Identify the blood parasite species.
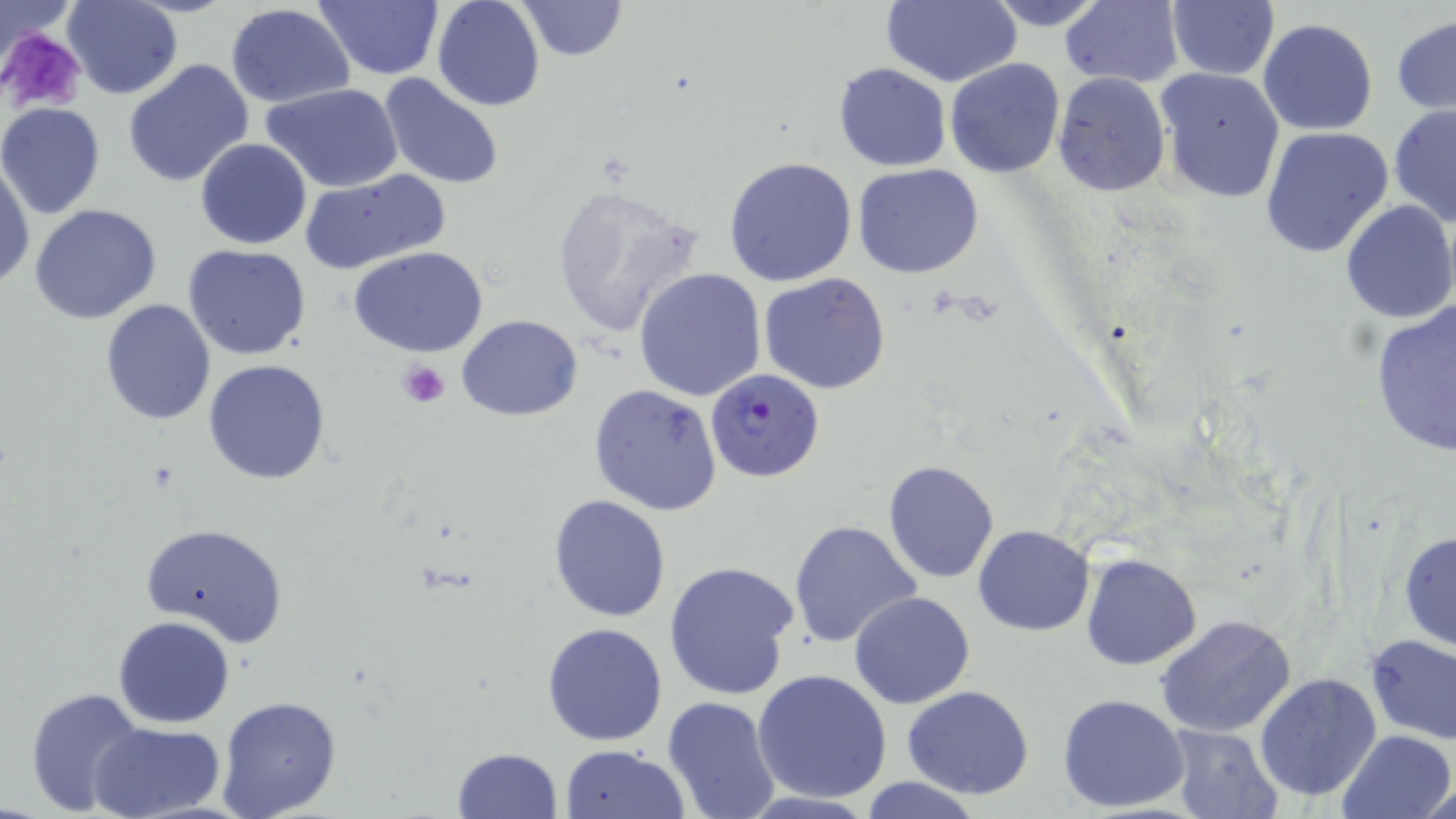

Plasmodium falciparum.

uninfected_red_blood_cell_locations: 'approximate bounding boxes as (x1, y1, x2, y2) in pixels: (315, 0, 443, 79), (432, 0, 545, 111), (517, 0, 627, 61), (883, 0, 1023, 86), (978, 0, 1115, 30), (1060, 0, 1183, 86), (63, 1, 181, 99), (1166, 2, 1280, 79), (225, 4, 355, 108), (1391, 16, 1455, 116), (1257, 18, 1379, 135), (944, 58, 1066, 177), (121, 59, 255, 189), (833, 64, 951, 171), (1153, 67, 1286, 204), (377, 73, 505, 192), (1052, 73, 1171, 198), (263, 83, 406, 194), (0, 103, 106, 219), (1388, 104, 1456, 230), (1260, 126, 1394, 257), (194, 139, 312, 250), (0, 156, 35, 292), (724, 156, 859, 286), (851, 162, 986, 278), (297, 169, 450, 275), (548, 183, 702, 338), (1339, 200, 1455, 323), (28, 203, 162, 324), (183, 245, 311, 361), (348, 246, 488, 358), (634, 266, 767, 401), (115, 272, 290, 404), (759, 272, 890, 394), (100, 298, 216, 425), (1369, 301, 1456, 457), (456, 315, 583, 420), (204, 358, 330, 485), (589, 383, 723, 517), (883, 460, 1000, 584), (549, 495, 671, 623), (789, 519, 922, 650), (140, 522, 288, 647), (973, 524, 1095, 635), (1397, 528, 1456, 654), (1079, 553, 1202, 670), (663, 560, 799, 701), (849, 592, 976, 709), (1155, 614, 1296, 738), (113, 615, 234, 728), (542, 622, 668, 746), (1364, 632, 1456, 745), (752, 668, 892, 803), (1254, 672, 1384, 802), (901, 685, 1034, 799), (24, 686, 145, 816), (1057, 692, 1191, 812), (217, 696, 342, 818), (661, 696, 782, 819), (89, 722, 226, 817), (1168, 724, 1284, 818), (1336, 729, 1455, 819), (558, 743, 690, 819), (450, 747, 562, 819), (859, 777, 985, 818), (1421, 779, 1454, 818)'
plasmodium_falciparum_infected_red_blood_cell_locations: 'approximate bounding boxes as (x1, y1, x2, y2) in pixels: (705, 368, 824, 484)'
stain: May-Grünwald-Giemsa
platelet_locations: 'approximate bounding boxes as (x1, y1, x2, y2) in pixels: (0, 28, 87, 116), (399, 359, 449, 408)'
image_size: 1456×819 pixels
field_of_view: single
modality: light microscopy
magnification: 1000x
preparation: thin blood smear